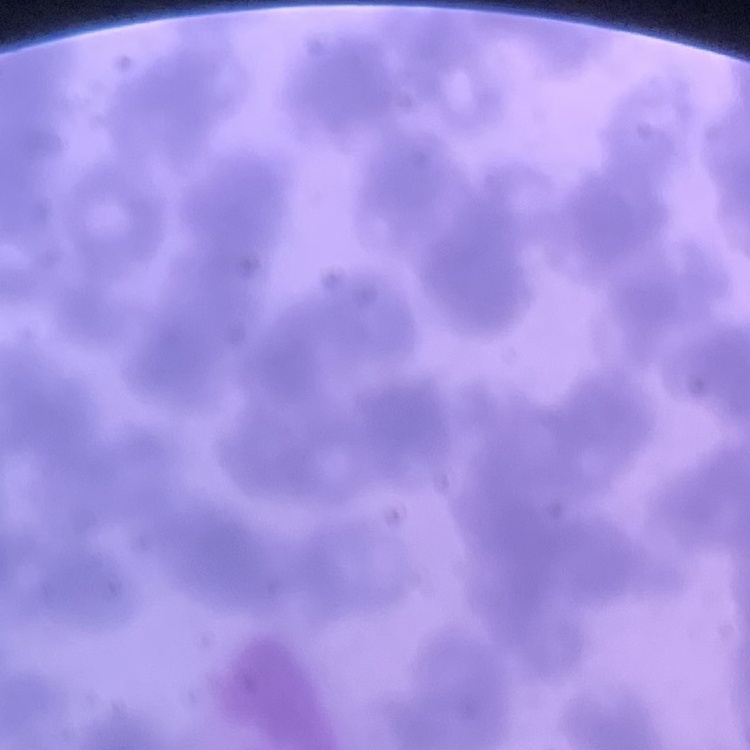
Summary:
  - Red blood cell morphology: rouleaux formation
  - Image type: one tile cut from a larger photomicrograph
  - Preparation: thin blood smear
  - Stain: Field's or Giemsa